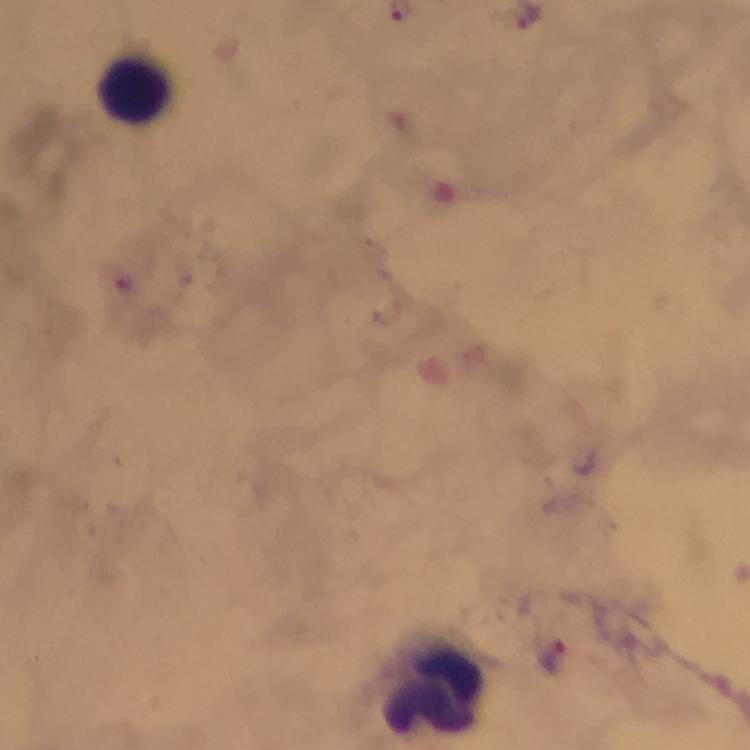

image size = 750×750 pixels
capture = smartphone photograph through a microscope
cropped from = a single field of view
context = from a diagnostic examination for malaria
stain = Giemsa
preparation = thick blood smear
magnification = 100x
immersion oil = used
Plasmodium parasite locations = approximate object centers, in pixels from the top-left corner: (x=550, y=656)
leukocyte locations = approximate object centers, in pixels from the top-left corner: (x=134, y=88), (x=432, y=691)